Report the malaria status of this cell.
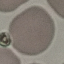

It is uninfected.

stain = Giemsa
image type = automatically extracted cell patch, resized to 64 × 64 pixels
capture = smartphone through the microscope eyepiece
preparation = thin smear